Outline each Plasmodium falciparum-infected red blood cell.
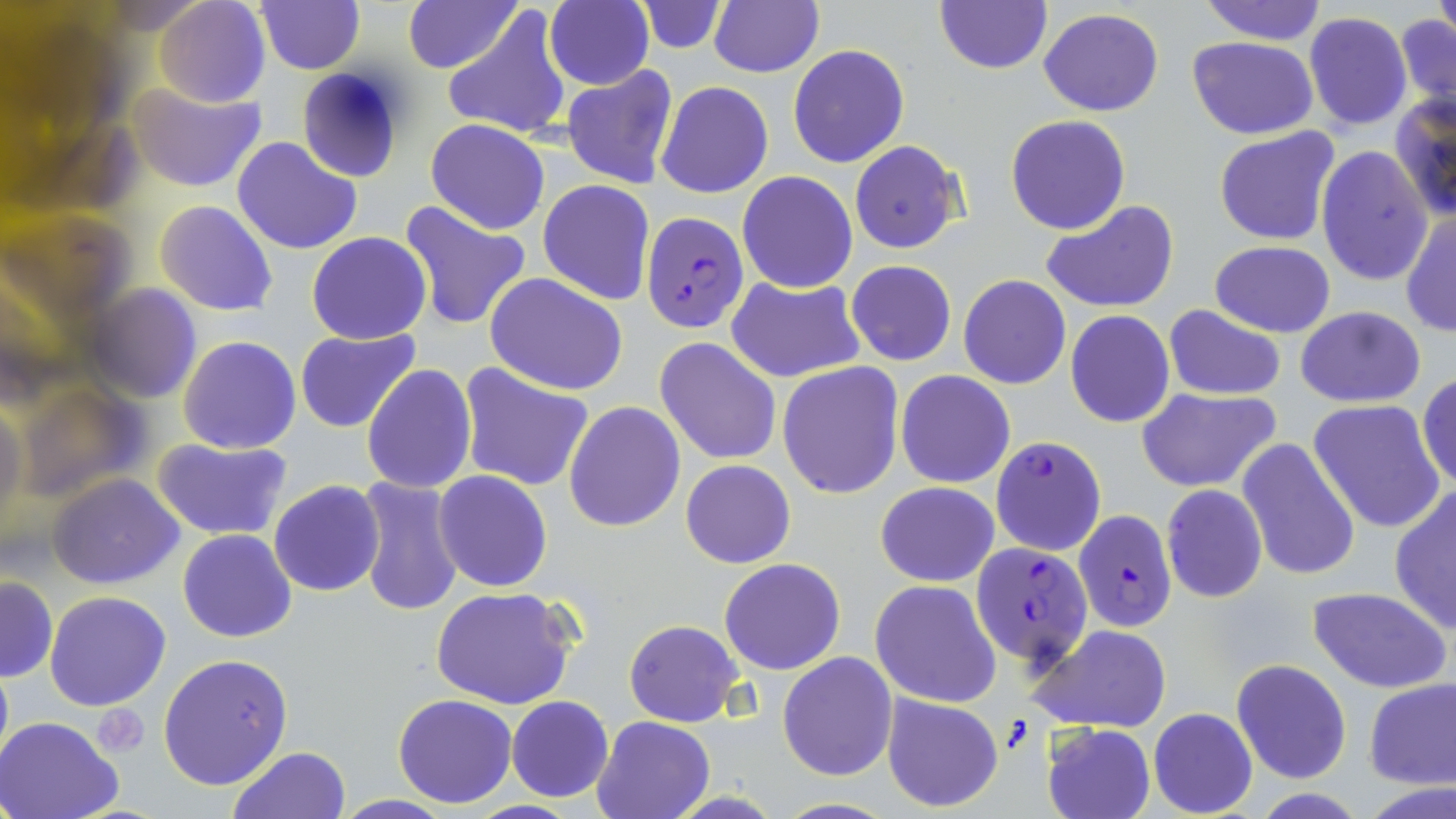

Approximate bounding boxes as [x1, y1, x2, y2] in pixels.
Plasmodium falciparum-infected red blood cells: [640, 212, 750, 334], [991, 436, 1106, 556], [1071, 508, 1177, 632], [971, 540, 1093, 672].

Uninfected red blood cell locations: [0, 0, 125, 134], [154, 0, 271, 107], [255, 0, 364, 74], [402, 0, 521, 72], [709, 0, 824, 79], [934, 0, 1052, 75], [1433, 0, 1455, 43], [1198, 1, 1328, 45], [544, 2, 655, 89], [633, 2, 728, 53], [442, 6, 570, 139], [1038, 8, 1163, 116], [1395, 10, 1455, 118], [1304, 11, 1413, 131], [1188, 36, 1317, 139], [788, 44, 909, 166], [297, 67, 404, 181], [562, 67, 679, 190], [655, 81, 773, 199], [130, 83, 268, 194], [1390, 93, 1455, 222], [1005, 115, 1131, 234], [425, 119, 549, 234], [1214, 127, 1343, 246], [232, 136, 362, 257], [849, 140, 965, 253], [1317, 145, 1433, 287], [737, 171, 858, 292], [538, 180, 655, 305], [398, 199, 533, 330], [1041, 199, 1179, 313], [156, 200, 276, 316], [0, 202, 134, 331], [1400, 211, 1456, 339], [307, 231, 431, 345], [1209, 241, 1335, 336], [846, 260, 956, 366], [485, 272, 629, 395], [959, 274, 1071, 390], [725, 275, 865, 384], [86, 285, 201, 404], [1163, 306, 1286, 399], [1296, 306, 1426, 407], [1066, 310, 1175, 428], [295, 328, 420, 433], [179, 336, 301, 454], [655, 337, 782, 465], [778, 362, 904, 500], [457, 363, 594, 493], [361, 365, 477, 494], [895, 370, 1016, 489], [1417, 371, 1456, 492], [16, 380, 149, 502], [1136, 387, 1282, 494], [1308, 400, 1446, 534], [0, 401, 26, 532], [564, 402, 685, 534], [154, 437, 294, 541], [1236, 437, 1363, 582], [681, 459, 795, 567], [433, 470, 555, 592], [47, 474, 184, 590], [354, 475, 465, 617], [269, 480, 385, 596], [875, 482, 1000, 585], [1161, 484, 1268, 603], [1389, 484, 1456, 634], [177, 529, 296, 643], [719, 558, 846, 676], [0, 576, 58, 682], [870, 580, 1003, 706], [430, 587, 576, 711], [1307, 587, 1452, 694], [45, 590, 171, 712], [624, 620, 744, 727], [1028, 624, 1171, 732], [777, 651, 898, 781], [157, 653, 294, 792], [0, 656, 12, 775], [1232, 659, 1352, 784], [1363, 678, 1456, 788], [393, 693, 519, 808], [881, 693, 1003, 814], [506, 696, 613, 802], [1148, 707, 1258, 818], [0, 715, 124, 819], [591, 715, 713, 819], [1042, 723, 1155, 819], [229, 746, 348, 819], [332, 795, 457, 818], [770, 798, 899, 817]. Slide-level diagnosis: Plasmodium falciparum. Image is 1456×819 pixels. Optical microscopy. 1000x magnification. Thin blood smear. One field of a larger specimen. May-Grünwald-Giemsa stain.